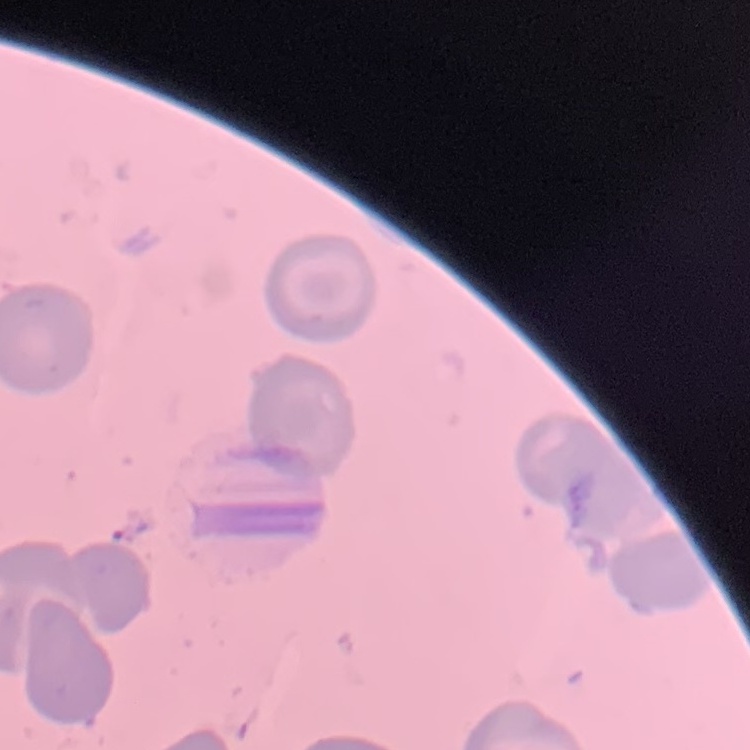

erythrocyte morphology = no rouleaux formation
stain = Field's or Giemsa
image type = one tile cut from a larger photomicrograph
preparation = thin blood film